Evaluate for Plasmodium parasites.
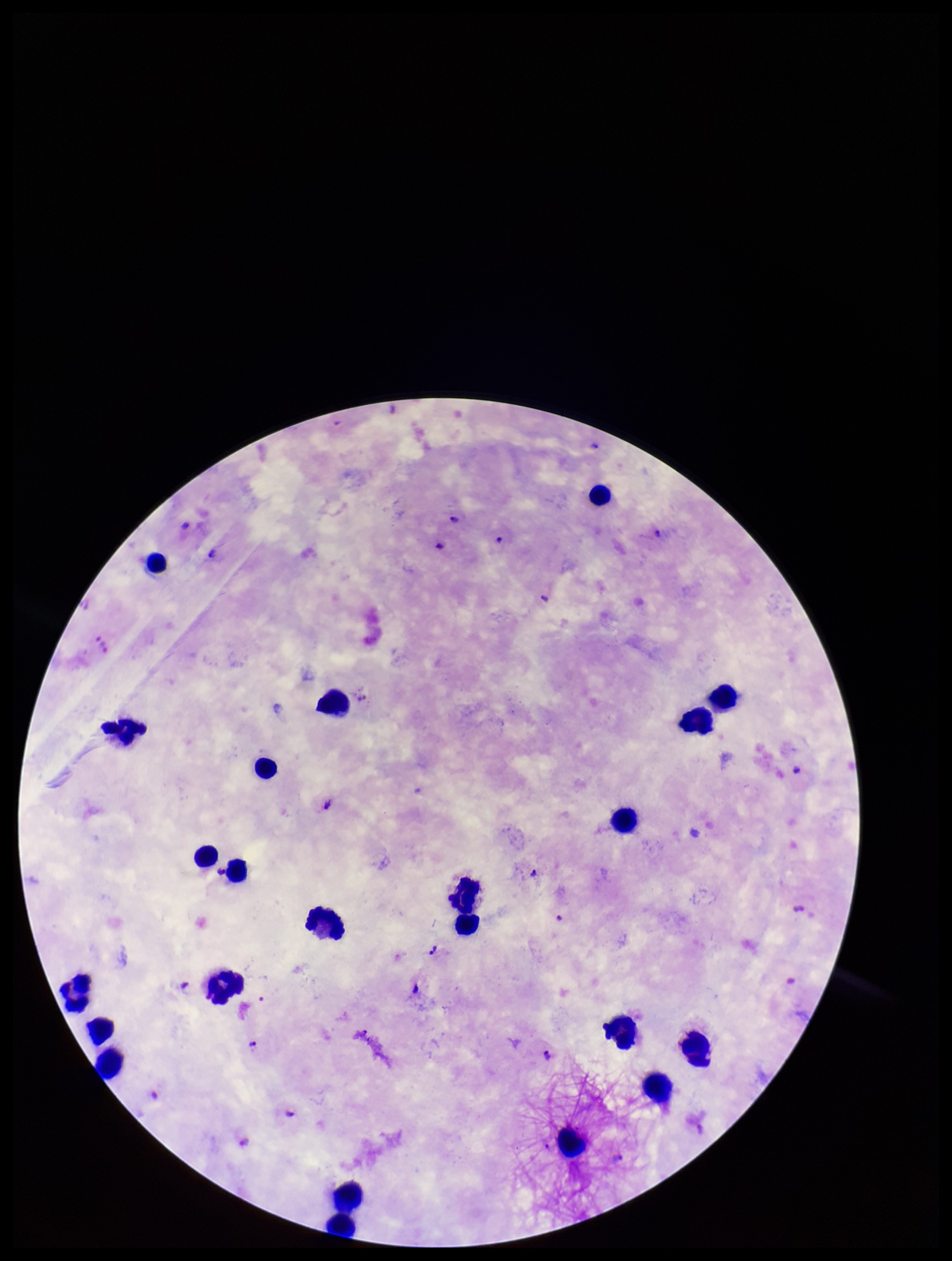
Identified.

Species reported for this patient: Plasmodium falciparum. Patient malaria status: infected. Single field of view. Image is 952×1261 pixels. Photographed through the microscope eyepiece with a smartphone camera. Stained with Giemsa. Parasite count: 10. Leukocyte count: 23. Preparation: thick.